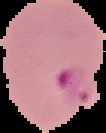 From a thin blood film. Result: Plasmodium parasites identified. Image is 106×133 pixels. Segmented cell region on a black background.